Give the extent of all Plasmodium falciparum-infected red blood cells.
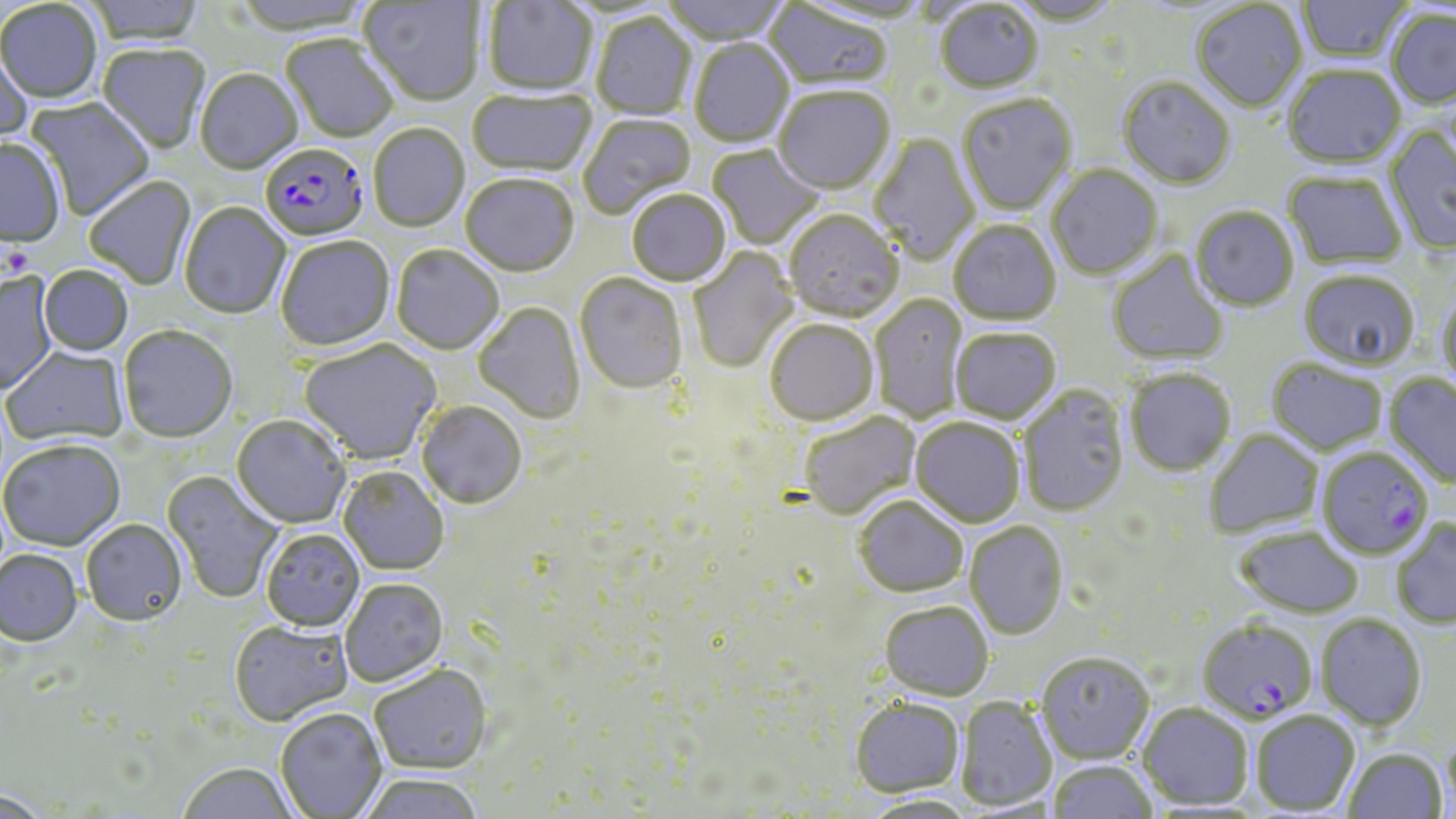

Approximate bounding boxes as (x1, y1, x2, y2) in pixels.
Plasmodium falciparum-infected red blood cells: (260, 144, 368, 243), (1321, 448, 1433, 558), (1197, 617, 1317, 723).

Uninfected red blood cell locations: (84, 0, 206, 47), (657, 0, 792, 45), (1297, 0, 1411, 64), (359, 1, 483, 107), (483, 1, 598, 97), (1005, 1, 1125, 28), (0, 2, 102, 105), (764, 2, 894, 93), (1192, 2, 1309, 114), (934, 3, 1044, 96), (1385, 10, 1456, 111), (591, 14, 697, 120), (281, 36, 398, 145), (689, 40, 794, 149), (0, 42, 34, 148), (96, 45, 210, 155), (1282, 67, 1407, 171), (196, 70, 303, 175), (1116, 78, 1236, 191), (467, 89, 596, 178), (774, 89, 895, 196), (957, 96, 1077, 217), (24, 97, 156, 220), (578, 114, 697, 218), (369, 125, 469, 232), (1383, 126, 1456, 255), (869, 133, 980, 267), (0, 140, 66, 248), (705, 145, 827, 251), (1047, 167, 1163, 280), (1282, 172, 1407, 271), (461, 175, 578, 277), (84, 177, 196, 291), (627, 190, 731, 287), (180, 203, 291, 319), (1190, 207, 1299, 312), (783, 211, 904, 323), (948, 220, 1061, 326), (276, 236, 395, 350), (392, 245, 504, 354), (688, 247, 799, 374), (1107, 250, 1230, 365), (38, 266, 133, 357), (1298, 271, 1420, 372), (0, 272, 59, 396), (575, 273, 688, 393), (1438, 290, 1456, 394), (869, 294, 967, 424), (474, 302, 585, 423), (765, 319, 878, 425), (118, 325, 238, 443), (950, 328, 1061, 424), (299, 340, 441, 464), (2, 347, 129, 447), (1266, 359, 1388, 456), (1124, 368, 1236, 476), (1383, 373, 1456, 489), (1017, 386, 1129, 516), (416, 400, 527, 508), (797, 412, 920, 519), (231, 415, 352, 528), (911, 417, 1025, 527), (1203, 429, 1324, 538), (0, 439, 126, 552), (339, 466, 449, 574), (161, 470, 286, 604), (854, 495, 968, 597), (1390, 518, 1456, 629), (81, 519, 187, 627), (964, 521, 1068, 639), (1235, 526, 1364, 617), (261, 529, 365, 631), (0, 550, 83, 647), (340, 578, 447, 686), (879, 600, 994, 700), (1316, 614, 1428, 731), (229, 620, 353, 725), (1036, 651, 1154, 762), (369, 665, 493, 774), (956, 696, 1056, 811), (850, 697, 964, 796), (1138, 703, 1253, 809), (275, 708, 386, 817), (1251, 710, 1360, 815), (1442, 728, 1456, 818), (1343, 747, 1448, 818), (1048, 759, 1157, 818), (176, 763, 299, 819), (356, 773, 487, 819), (0, 789, 54, 819), (860, 794, 980, 818). Slide-level diagnosis: Plasmodium falciparum. Optical microscopy. Thin blood smear. 1000x magnification. Image is 1456×819 pixels. One field of a larger specimen. May-Grünwald-Giemsa stain.